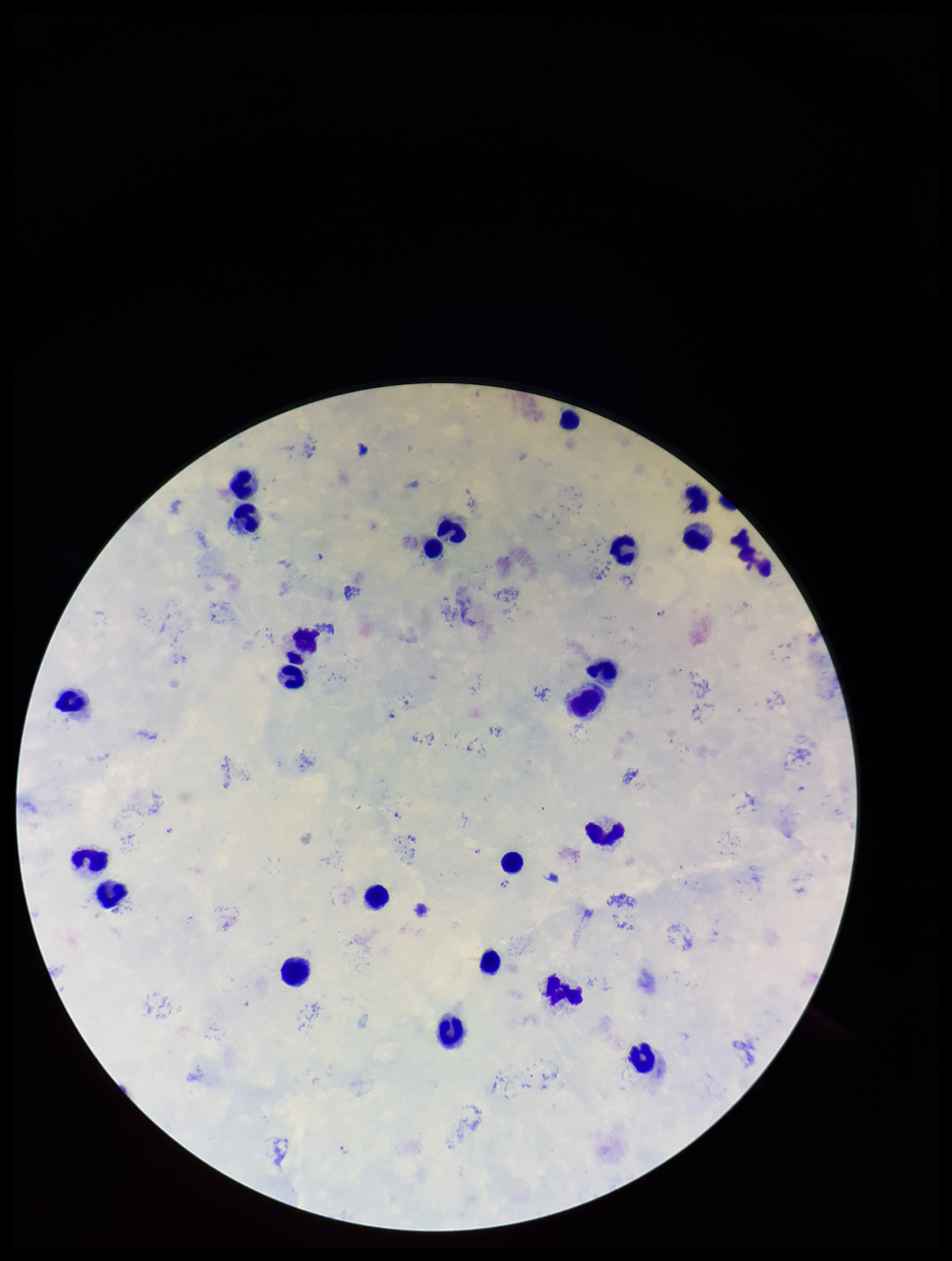

stain = Giemsa
field of view = single
species reported for this patient = Plasmodium falciparum
patient malaria status = positive
parasite count = 5
Plasmodium parasites = seen
leukocyte count = 24
image size = 952×1261 pixels
capture = smartphone photograph through the microscope eyepiece
preparation = thick blood smear